Locate every Plasmodium parasite.
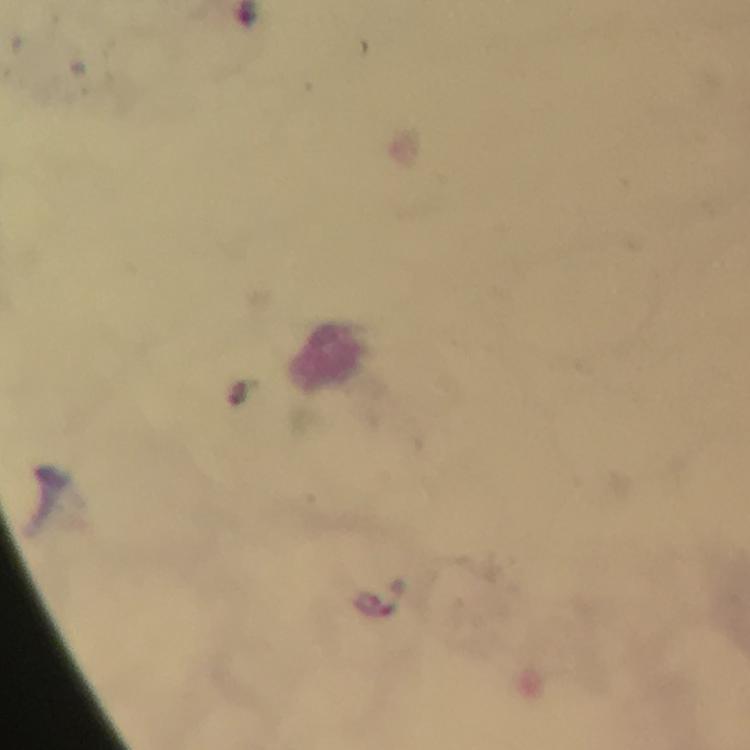

Approximate object centers, in pixels from the top-left corner.
Plasmodium parasites: (x=247, y=12), (x=393, y=597).

Summary:
  - Context: from a diagnostic examination for malaria
  - Immersion oil: applied
  - Stain: Giemsa
  - Cropped from: a single field of view
  - Magnification: 100x
  - Capture: smartphone mounted on the microscope
  - Image size: 750×750 pixels
  - Preparation: thick smear